State which parasite is depicted.
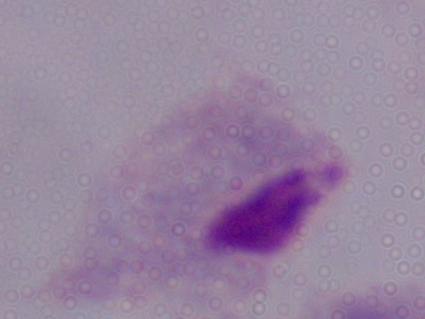
This is a trichomonad.

magnification: 1000x
modality: micrograph